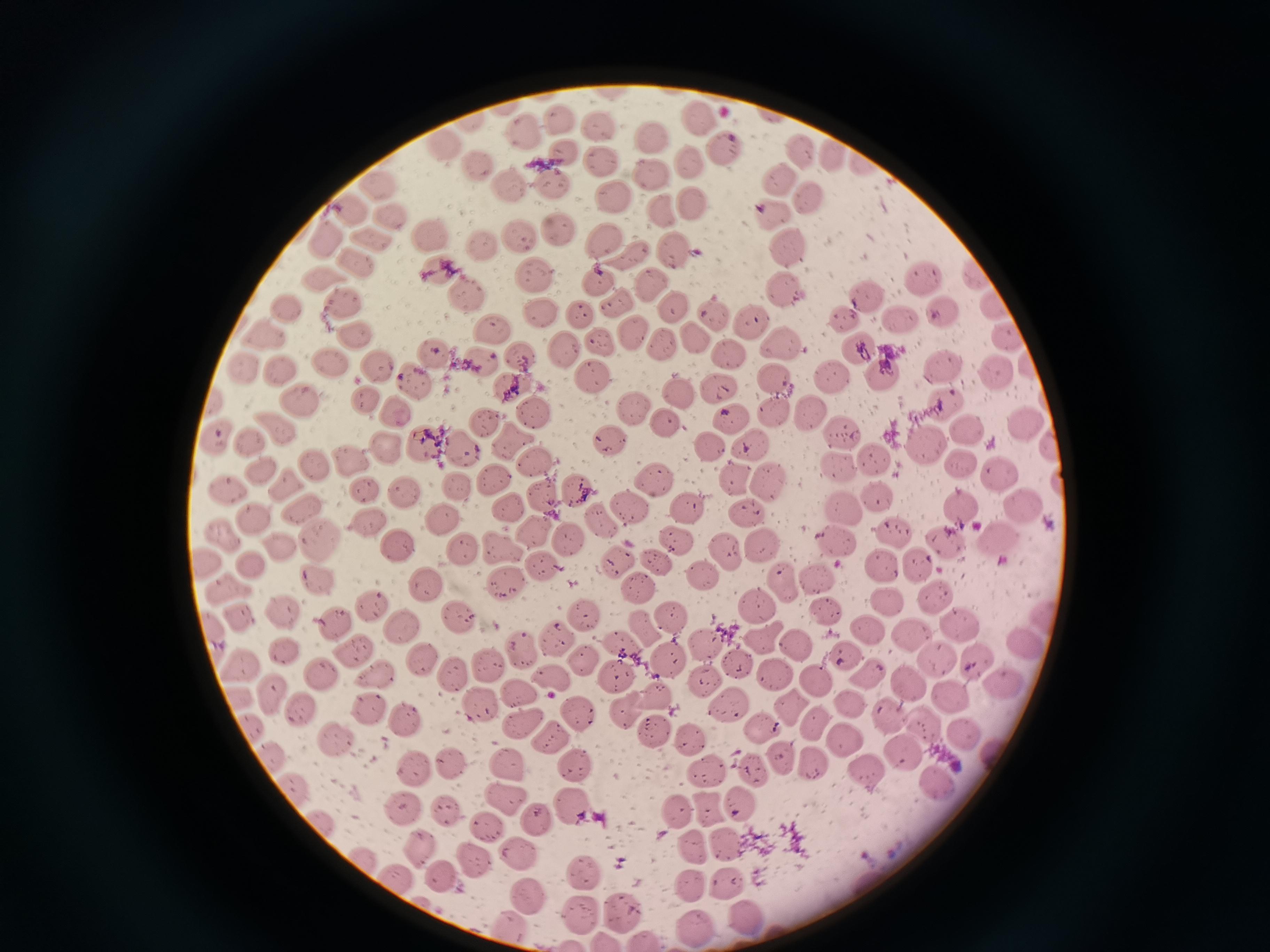

Approximate centers as {x, y} in pixels.
Summary:
  - Cell locations: {502, 108}, {695, 117}, {559, 120}, {470, 121}, {601, 124}, {522, 131}, {650, 138}, {442, 144}, {726, 150}, {828, 151}, {800, 153}, {563, 154}, {599, 162}, {688, 164}, {480, 167}, {651, 174}, {777, 177}, {511, 183}, {548, 183}, {376, 184}, {612, 196}, {807, 197}, {690, 201}, {354, 207}, {663, 209}, {771, 214}, {393, 216}, {559, 228}, {431, 235}, {518, 235}, {373, 236}, {327, 237}, {601, 240}, {790, 246}, {482, 247}, {674, 255}, {629, 258}, {358, 262}, {433, 270}, {977, 273}, {534, 275}, {320, 277}, {922, 277}, {600, 279}, {651, 282}, {785, 286}, {465, 291}, {866, 297}, {618, 301}, {346, 304}, {675, 306}, {996, 308}, {284, 309}, {578, 313}, {712, 313}, {945, 313}, {539, 315}, {749, 318}, {844, 320}, {901, 321}, {492, 328}, {634, 331}, {262, 334}, {353, 335}, {1010, 335}, {693, 337}, {600, 343}, {665, 344}, {780, 345}, {563, 350}, {853, 351}, {432, 353}, {519, 353}, {729, 354}, {328, 360}, {377, 367}, {946, 367}, {284, 369}, {245, 371}, {880, 375}, {831, 376}, {1000, 376}, {592, 377}, {412, 379}, {776, 379}, {514, 386}, {721, 386}, {679, 393}, {365, 397}, {297, 399}, {213, 401}, {946, 401}, {632, 407}, {397, 410}, {774, 410}, {535, 411}, {808, 417}, {732, 420}, {485, 422}, {667, 423}, {1025, 424}, {273, 427}, {967, 430}, {841, 433}, {251, 438}, {510, 440}, {611, 440}, {217, 441}, {749, 442}, {423, 445}, {709, 446}, {925, 446}, {465, 447}, {386, 449}, {347, 459}, {877, 459}, {534, 461}, {963, 462}, {311, 464}, {838, 465}, {258, 468}, {1001, 473}, {733, 478}, {770, 479}, {494, 480}, {652, 480}, {282, 484}, {458, 484}, {365, 490}, {405, 491}, {578, 491}, {224, 493}, {879, 495}, {544, 498}, {1023, 504}, {841, 506}, {631, 508}, {305, 509}, {506, 509}, {690, 510}, {965, 510}, {748, 515}, {253, 517}, {367, 519}, {440, 519}, {220, 532}, {535, 533}, {891, 534}, {679, 536}, {998, 538}, {321, 539}, {569, 539}, {835, 542}, {945, 542}, {274, 545}, {763, 545}, {498, 547}, {396, 548}, {463, 548}, {726, 553}, {614, 558}, {247, 562}, {654, 562}, {206, 565}, {542, 565}, {880, 565}, {920, 565}, {702, 575}, {317, 578}, {817, 578}, {423, 585}, {504, 585}, {643, 587}, {786, 587}, {226, 589}, {934, 594}, {887, 599}, {368, 605}, {755, 605}, {281, 612}, {828, 614}, {581, 615}, {238, 616}, {455, 616}, {672, 617}, {1041, 618}, {332, 622}, {642, 625}, {957, 625}, {398, 628}, {866, 632}, {909, 633}, {557, 636}, {214, 638}, {763, 638}, {1019, 641}, {795, 643}, {624, 646}, {707, 647}, {282, 650}, {347, 650}, {518, 650}, {848, 656}, {977, 658}, {421, 659}, {582, 661}, {668, 661}, {738, 661}, {939, 663}, {240, 665}, {490, 666}, {451, 673}, {318, 674}, {614, 674}, {779, 674}, {867, 674}, {379, 678}, {549, 678}, {1000, 680}, {707, 681}, {815, 682}, {909, 684}, {519, 693}, {272, 694}, {947, 695}, {658, 696}, {237, 698}, {850, 704}, {726, 705}, {789, 705}, {475, 707}, {300, 709}, {369, 710}, {624, 710}, {577, 714}, {890, 715}, {403, 719}, {521, 721}, {813, 723}, {925, 723}, {254, 726}, {762, 729}, {654, 733}, {962, 734}, {554, 737}, {689, 737}, {843, 740}, {337, 741}, {904, 751}, {270, 757}, {782, 759}, {447, 762}, {509, 764}, {815, 764}, {412, 765}, {579, 767}, {702, 769}, {753, 771}, {864, 773}, {938, 784}, {296, 790}, {506, 799}, {742, 800}, {573, 806}, {708, 807}, {400, 811}, {447, 812}, {676, 813}, {535, 820}, {322, 824}, {485, 824}, {416, 844}, {728, 844}, {693, 847}, {363, 857}, {520, 857}, {474, 862}, {585, 872}, {439, 875}, {395, 880}, {728, 881}, {690, 883}, {529, 897}, {578, 911}, {621, 913}, {745, 917}, {508, 925}, {693, 927}, {605, 941}, {646, 941}
  - Image size: 1270×952 pixels
  - Preparation: thin blood smear
  - Stain: Giemsa
  - Capture: smartphone through the microscope eyepiece
  - Field of view: single